Report the malaria status of this cell.
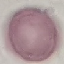
Uninfected.

stain: Giemsa
capture: smartphone camera at the microscope eyepiece
preparation: thin blood film
image_type: automatically extracted cell patch, resized to 64 × 64 pixels